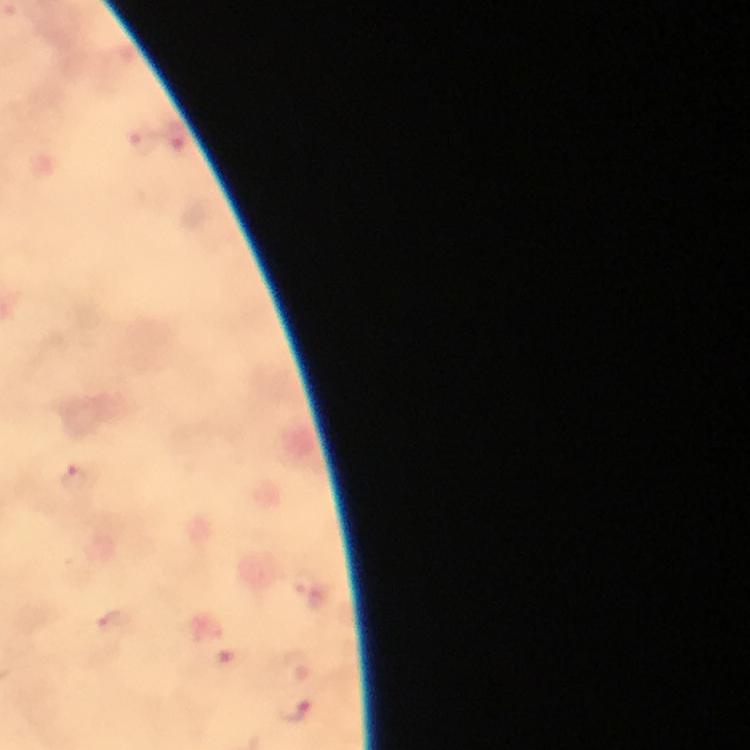

capture = smartphone photograph through a microscope
context = from a malaria diagnostic workup
malaria parasite locations = approximate centers as [x, y] in pixels: [178, 135], [142, 141], [72, 478], [295, 708]
preparation = thick smear
cropped from = a single field of view
stain = Giemsa
magnification = 100x
image size = 750×750 pixels
immersion oil = applied